Assess for Plasmodium parasites.
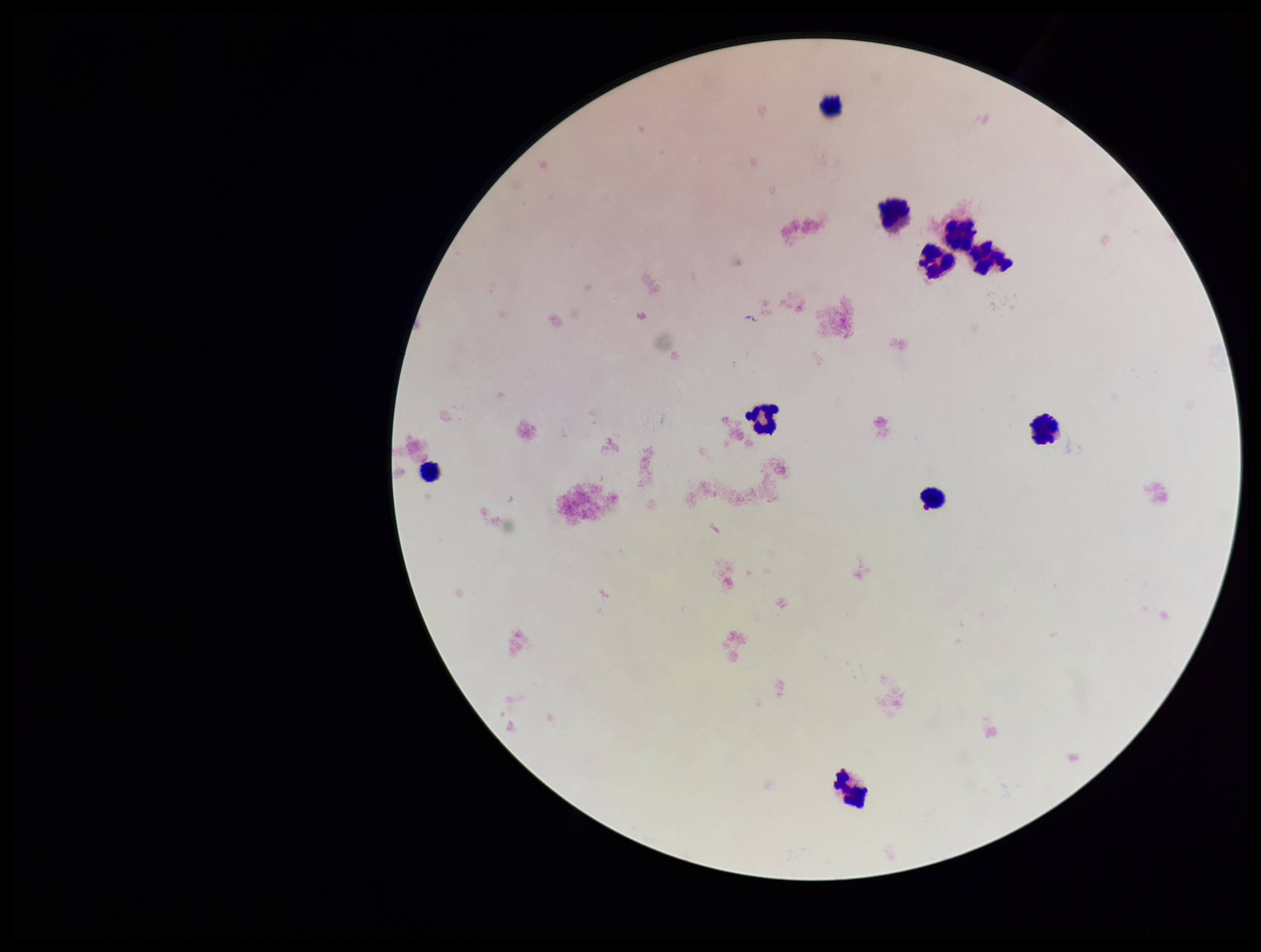

None seen.

Photographed through the microscope eyepiece with a smartphone camera. Preparation: thick smear. Parasite count: 0. Single field of view. Patient malaria status: negative. Stained with Giemsa. Image is 1261×952 pixels. Leukocyte count: 10.